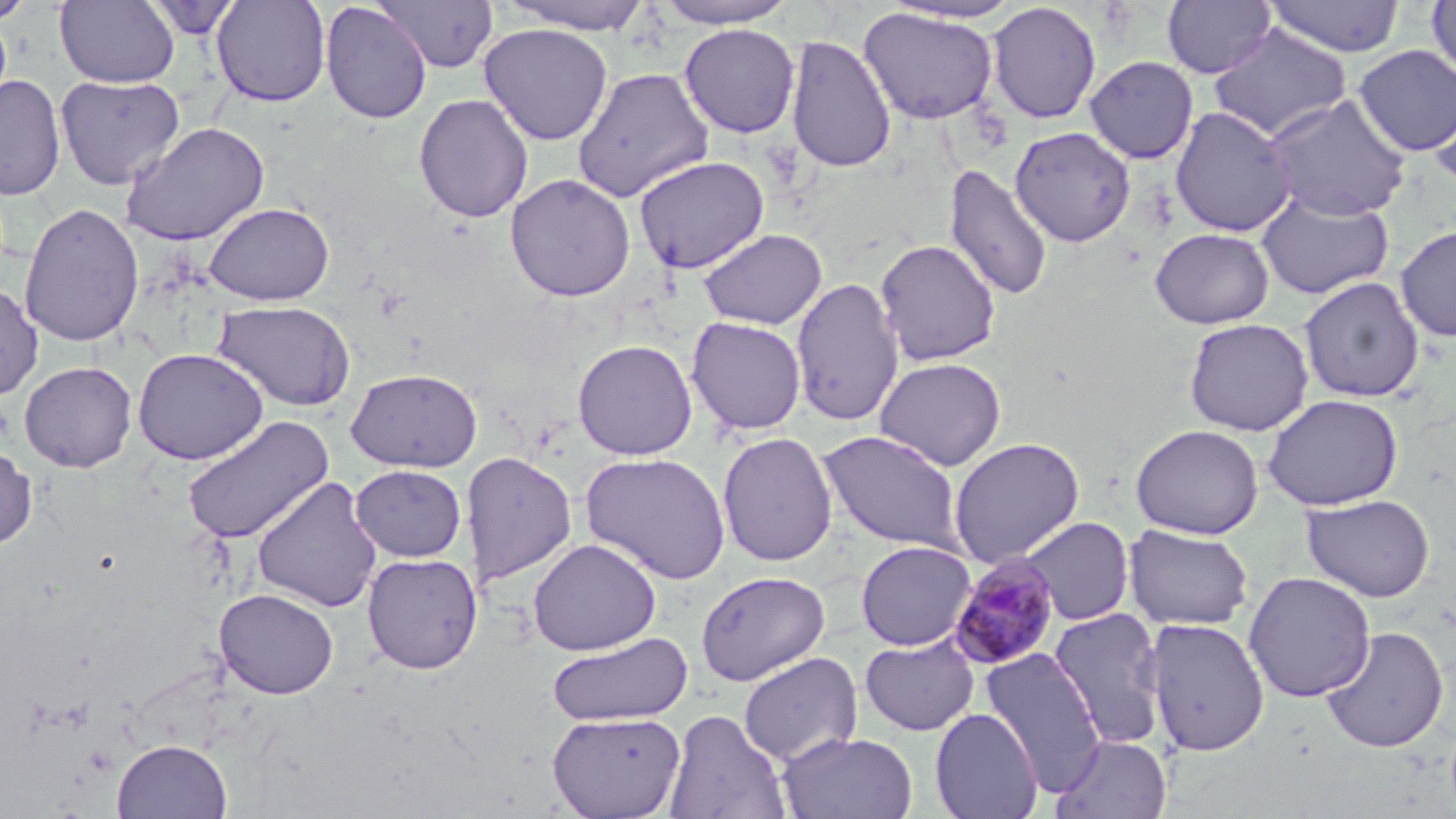 Approximate bounding boxes as (x1,y1)-(x2,y2) corner pairs in pixels. Plasmodium malariae-infected red blood cell locations: (947,553)-(1063,671). Uninfected red blood cell locations: (0,0)-(37,24), (55,0)-(179,88), (144,0)-(242,39), (372,0)-(499,73), (654,0)-(799,28), (1162,0)-(1276,79), (1263,0)-(1405,58), (211,1)-(331,106), (499,1)-(656,35), (880,1)-(1025,24), (1426,1)-(1456,84), (320,2)-(432,124), (986,2)-(1102,124), (858,6)-(999,125), (479,23)-(613,145), (679,23)-(800,138), (1209,24)-(1353,142), (785,34)-(896,173), (1353,45)-(1456,157), (1085,56)-(1199,164), (572,67)-(714,203), (1427,73)-(1456,191), (0,75)-(66,201), (55,75)-(185,190), (413,93)-(534,223), (1265,93)-(1412,221), (1170,106)-(1296,237), (121,121)-(270,246), (1010,126)-(1136,248), (634,155)-(769,274), (944,163)-(1053,302), (505,173)-(636,302), (1255,190)-(1395,300), (203,201)-(335,306), (19,203)-(144,348), (1395,224)-(1456,342), (1149,227)-(1275,329), (698,228)-(827,330), (874,239)-(1001,366), (791,276)-(905,426), (1298,276)-(1425,403), (0,284)-(43,400), (214,300)-(356,412), (686,316)-(807,436), (1183,317)-(1314,437), (572,339)-(697,460), (132,347)-(268,465), (874,356)-(1007,471), (19,361)-(137,473), (345,368)-(483,473), (1262,393)-(1403,510), (183,415)-(334,545), (1130,423)-(1264,540), (818,429)-(966,552), (717,432)-(839,567), (948,437)-(1085,566), (0,446)-(38,550), (462,451)-(578,586), (580,452)-(731,584), (351,464)-(466,561), (252,476)-(382,613), (1301,494)-(1435,602), (1018,516)-(1135,626), (1123,525)-(1254,631), (529,538)-(662,656), (855,540)-(977,651), (362,553)-(483,674), (695,570)-(831,687), (1243,571)-(1377,703), (213,588)-(339,699), (1047,607)-(1170,749), (1144,617)-(1269,756), (1321,626)-(1449,753), (547,632)-(693,727), (860,636)-(980,736), (980,648)-(1107,794), (739,652)-(863,767), (929,707)-(1043,819), (663,708)-(791,818), (547,711)-(686,819), (778,731)-(918,819), (1052,733)-(1172,819), (112,739)-(232,818). Slide-level diagnosis: Plasmodium malariae. Thin blood smear. Captured at 1000x magnification. May-Grünwald-Giemsa-stained preparation. Image is 1456×819 pixels. One field of a larger specimen. Light microscopy.